Classify this cell by malaria status.
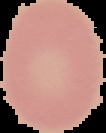
It is uninfected.

Summary:
  - Preparation: thin blood smear
  - Image size: 106×133 pixels
  - Image type: cell region segmented out of the field of view; surrounding area masked to black